Identify the parasite.
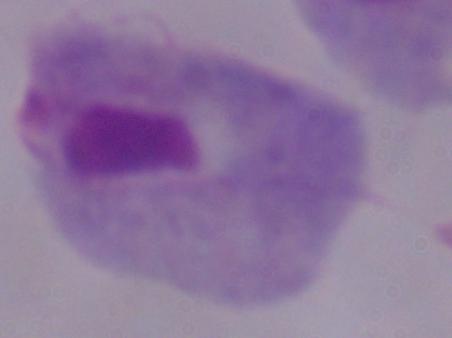

A trichomonad.

Captured at 1000x magnification. Micrograph.